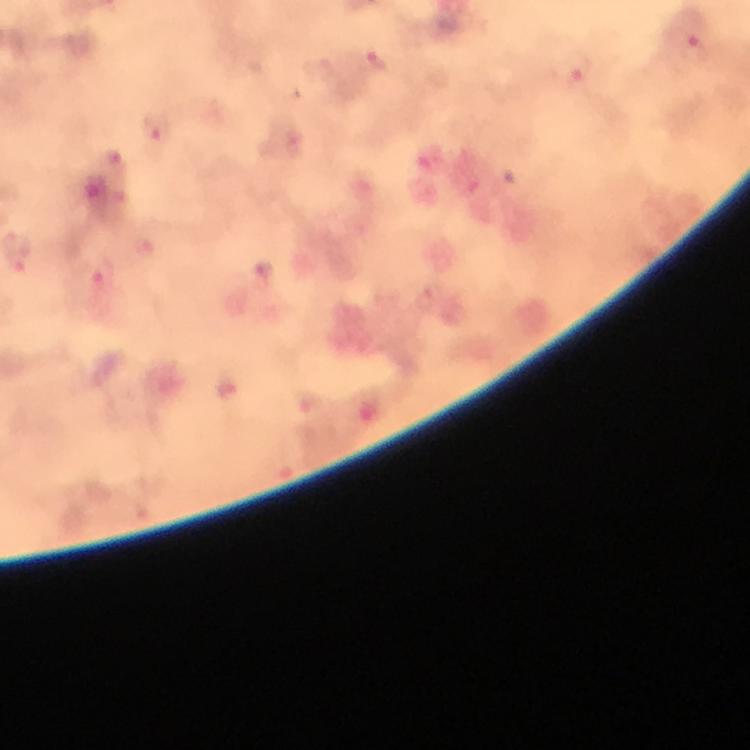
context = from a diagnostic examination for malaria
capture = smartphone photograph through a microscope
magnification = 100x
malaria parasite locations = approximate centers as [x, y] in pixels: [695, 48], [378, 63], [578, 69], [156, 128], [19, 255], [103, 281]
cropped from = a single field of view
immersion oil = applied
image size = 750×750 pixels
preparation = thick blood smear
stain = Giemsa